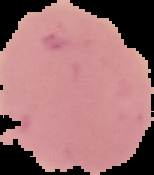 Result: negative for malaria parasites. The area outside the segmented cell region is set to black. Image is 154×175 pixels. From a thin blood film.